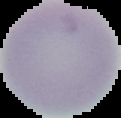
image_size: 121×118 pixels
malaria_status: uninfected
image_type: segmented cell region on a black background
preparation: thin blood smear